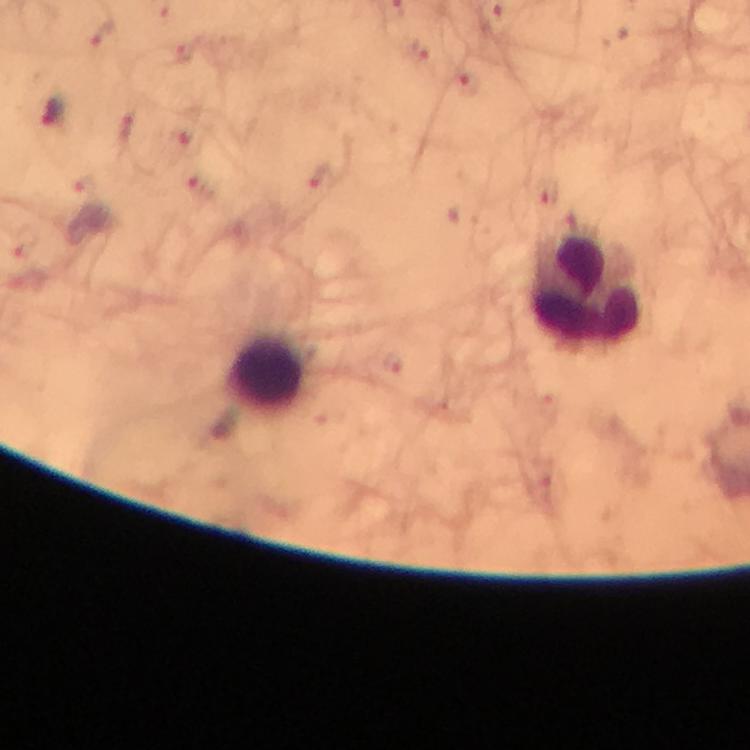

image size = 750×750 pixels
stain = Giemsa
capture = smartphone camera through the microscope
immersion oil = applied
cropped from = one field of view
magnification = 100x
leukocyte locations = approximate centers as [x, y] in pixels: [587, 291], [268, 371]
Plasmodium parasite locations = approximate centers as [x, y] in pixels: [466, 84], [54, 112]
preparation = thick blood smear
context = from a malaria diagnostic workup